Comment on the morphology of the erythrocytes.
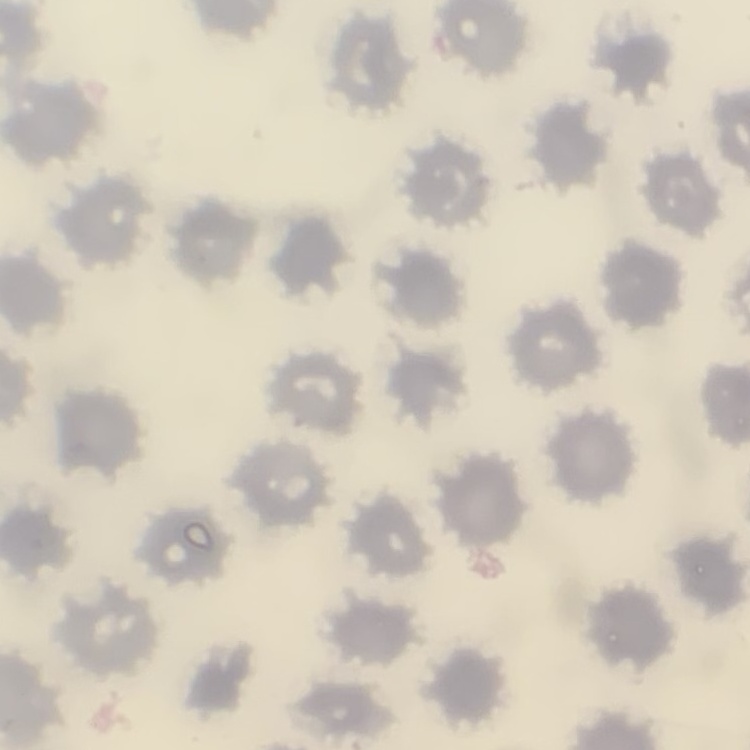
No rouleaux formation.

Stained with either Field's or Giemsa. Square crop of a larger photomicrograph. Thin blood smear.